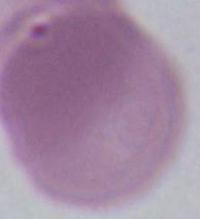

Captured at 1000x magnification. An erythrocyte is shown. Micrograph.